Report the malaria status of this cell.
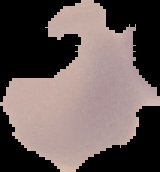
It is uninfected.

Summary:
  - Image type: segmented cell region on a black background
  - Preparation: thin blood film
  - Image size: 160×172 pixels